Report the malaria status of this cell.
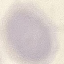
It is uninfected.

Summary:
  - Preparation: thin blood film
  - Image type: automatically extracted cell patch, resized to 64 × 64 pixels
  - Capture: smartphone through the microscope eyepiece
  - Stain: Giemsa